Report the malaria status of this cell.
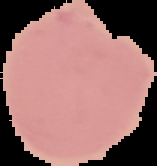
It is uninfected.

image type = cell region segmented out of the field of view; surrounding area masked to black
image size = 157×166 pixels
preparation = thin blood film